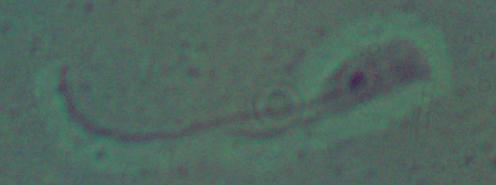

modality = photomicrograph
magnification = 1000x
identification = Leishmania